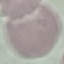 Result: no malaria parasites seen. Acquired by smartphone through the microscope eyepiece. Thin blood smear. Giemsa stain. Automatically extracted cell patch, resized to 64 × 64 pixels.